Classify this cell by malaria status.
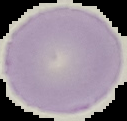
It is uninfected.

Summary:
  - Image size: 127×121 pixels
  - Image type: segmented cell region with the area outside set to black
  - Preparation: thin blood film